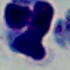 1000x magnification. Photomicrograph. A leukocyte is seen.